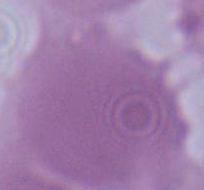

Summary:
  - Modality: photomicrograph
  - Magnification: 1000x
  - Identification: red blood cell